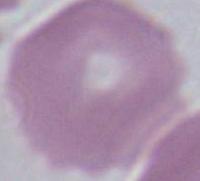
Summary:
  - Magnification: 1000x
  - Identification: red blood cell
  - Modality: photomicrograph